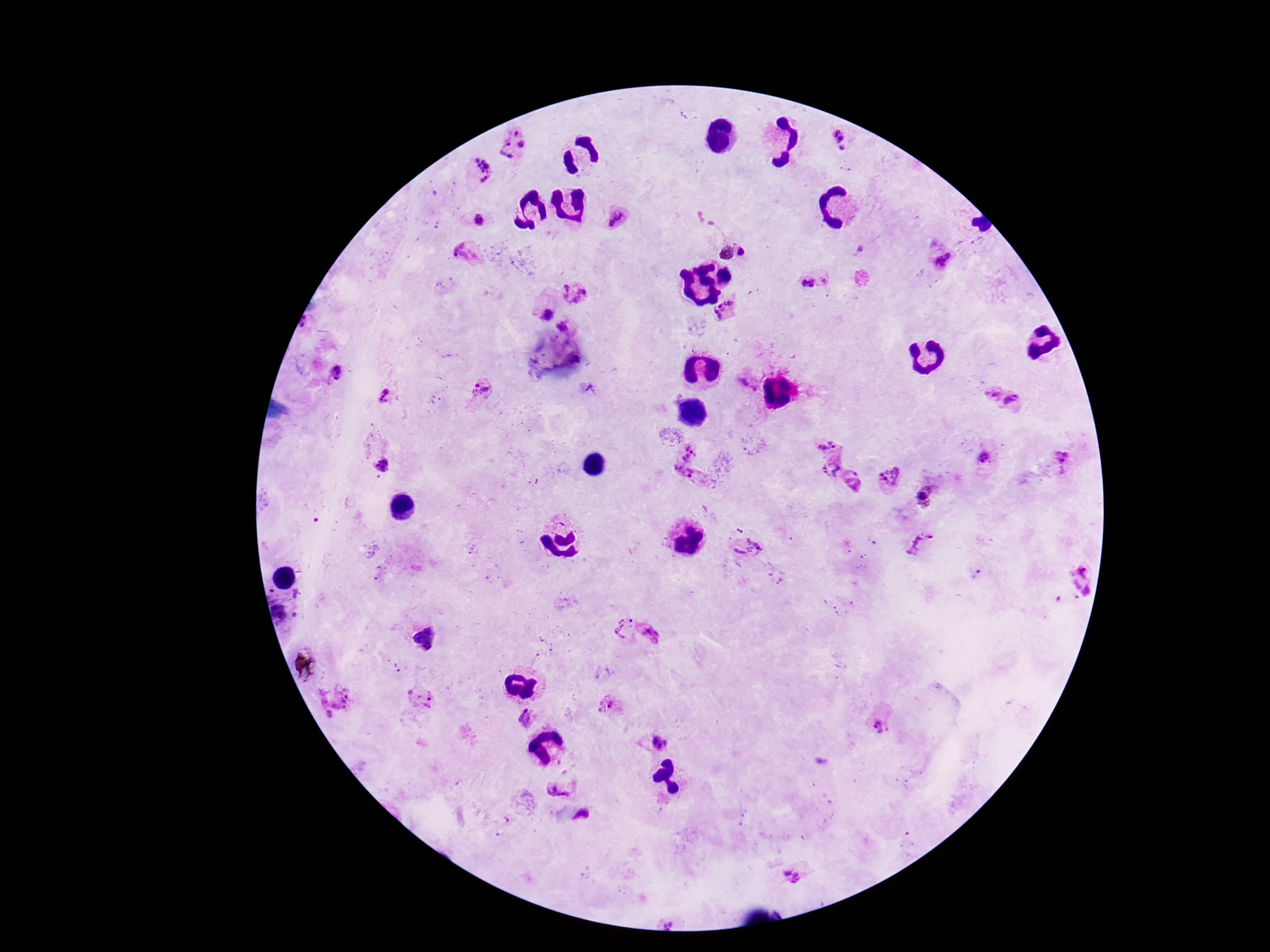

field of view = single
Plasmodium parasite locations = approximate centers as [x, y] in pixels: [839, 140], [510, 144], [474, 173], [618, 218], [478, 220], [724, 252], [743, 252], [468, 253], [946, 262], [815, 277], [574, 292], [726, 311], [545, 314], [565, 326], [338, 373], [745, 384], [483, 389], [385, 397], [1002, 399], [831, 440], [1063, 458], [984, 459], [688, 462], [381, 465], [830, 467], [853, 478], [890, 479], [929, 498], [920, 545], [746, 550], [1077, 576], [283, 609], [620, 627], [648, 633], [422, 694], [335, 699], [610, 707], [529, 720], [879, 725], [657, 740], [562, 787], [792, 876]
image size = 1270×952 pixels
capture = smartphone camera through the microscope eyepiece
preparation = thick blood film
patient malaria status = positive
stain = Giemsa
magnification = 100x